Point out each Plasmodium parasite.
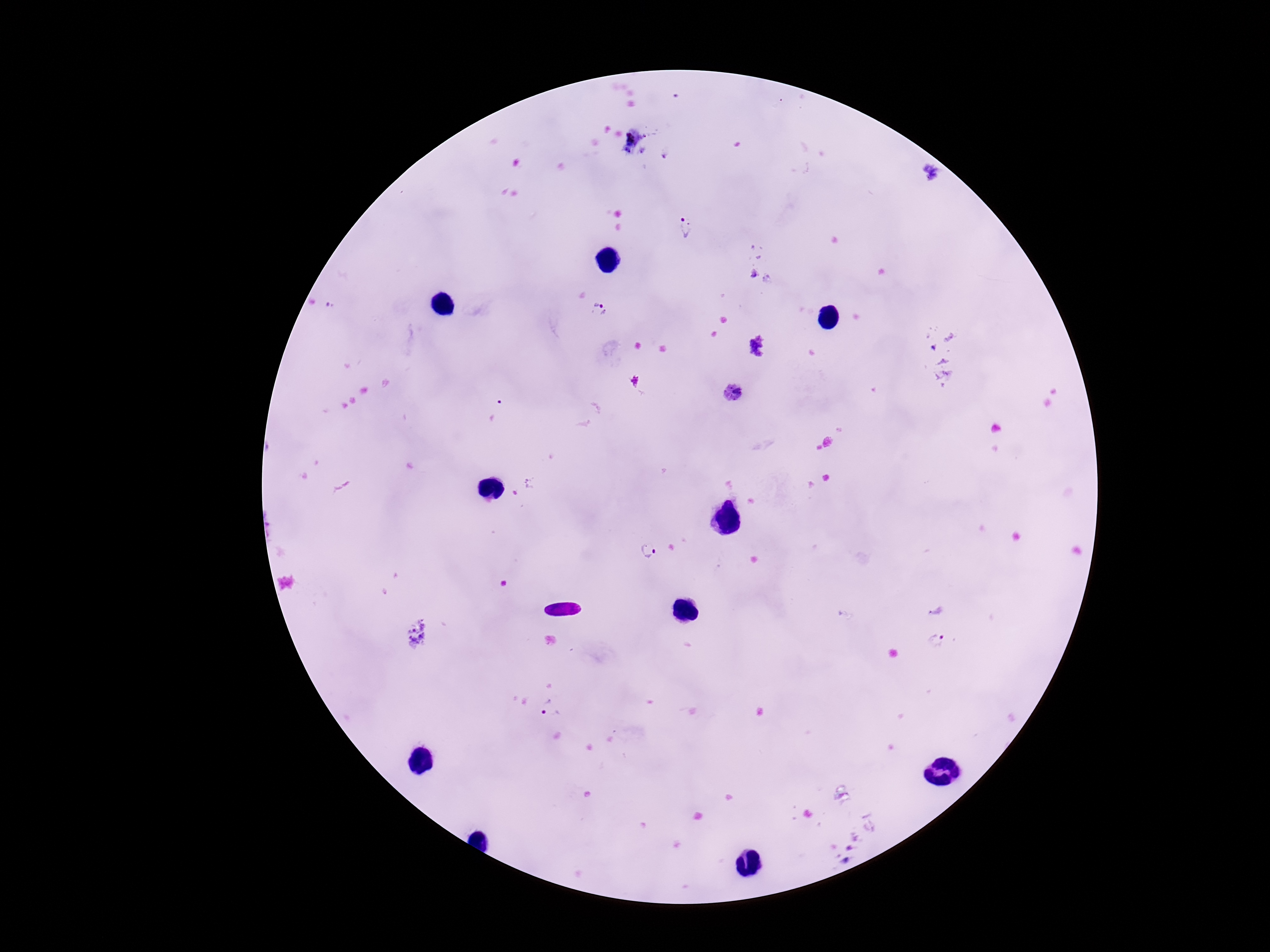
Approximate centers as [x, y] in pixels.
Plasmodium parasites: [666, 153], [684, 227], [753, 273], [596, 301], [332, 306], [756, 345], [735, 394], [495, 409], [649, 549], [935, 640], [549, 708].

Summary:
  - Magnification: 100x
  - Patient malaria status: infected
  - Field of view: single
  - Capture: smartphone camera through the microscope eyepiece
  - Image size: 1270×952 pixels
  - Stain: Giemsa
  - Preparation: thick peripheral-blood smear